Point out Plasmodium parasites and leukocytes.
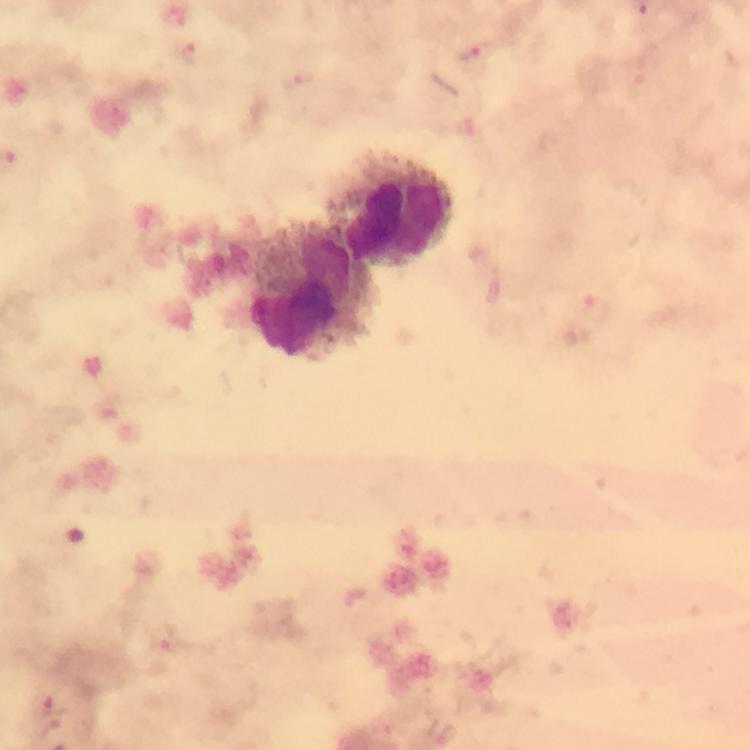
Approximate centers as [x, y] in pixels.
Plasmodium parasites: [193, 54], [476, 56], [302, 83], [597, 312], [170, 644], [52, 703], [51, 727], [442, 732].
Leukocytes: [395, 209], [311, 292].

Immersion oil applied. At 100x magnification. Giemsa stain. Photographed with a smartphone mounted on the microscope. Thick smear. From a malaria diagnostic workup. Image is 750×750 pixels. Cropped region of a single field of view.